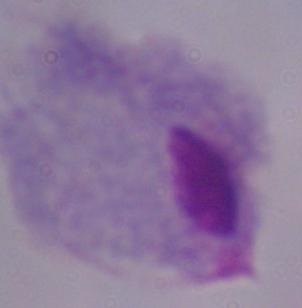
{
  "magnification": "1000x",
  "modality": "photomicrograph",
  "identification": "trichomonad"
}